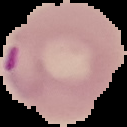 From a thin blood film. Cell region segmented out of the field of view; the surrounding area is masked to black. Result: Plasmodium parasites detected. Image is 127×127 pixels.